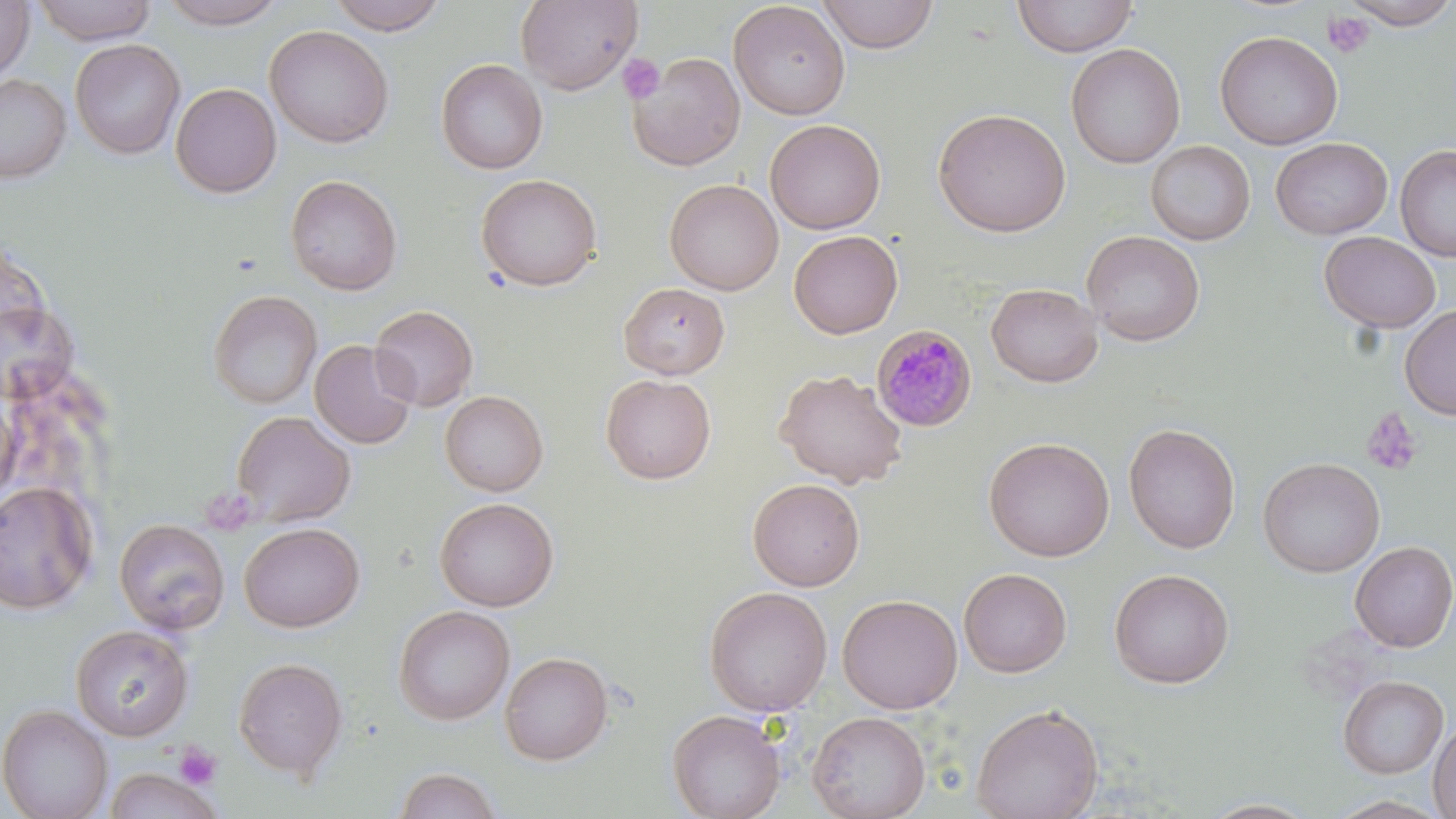
slide-level diagnosis = Plasmodium malariae
modality = optical microscopy
uninfected red blood cell locations = approximate bounding boxes as named x1/y1/x2/y2 corners in pixels: (x1=31, y1=0, x2=158, y2=45), (x1=155, y1=0, x2=288, y2=29), (x1=326, y1=0, x2=450, y2=35), (x1=515, y1=0, x2=641, y2=94), (x1=817, y1=0, x2=940, y2=53), (x1=1012, y1=0, x2=1138, y2=57), (x1=1342, y1=0, x2=1456, y2=29), (x1=0, y1=1, x2=34, y2=83), (x1=728, y1=1, x2=850, y2=120), (x1=264, y1=24, x2=394, y2=149), (x1=1214, y1=30, x2=1343, y2=150), (x1=70, y1=39, x2=185, y2=159), (x1=1066, y1=43, x2=1185, y2=168), (x1=628, y1=52, x2=746, y2=171), (x1=436, y1=59, x2=548, y2=174), (x1=0, y1=73, x2=71, y2=183), (x1=170, y1=82, x2=281, y2=198), (x1=932, y1=108, x2=1071, y2=237), (x1=765, y1=119, x2=885, y2=234), (x1=1270, y1=137, x2=1392, y2=239), (x1=1145, y1=140, x2=1255, y2=245), (x1=1395, y1=144, x2=1456, y2=263), (x1=476, y1=173, x2=603, y2=291), (x1=284, y1=174, x2=403, y2=295), (x1=665, y1=179, x2=783, y2=295), (x1=789, y1=230, x2=902, y2=339), (x1=1081, y1=230, x2=1205, y2=347), (x1=1319, y1=231, x2=1441, y2=333), (x1=618, y1=282, x2=730, y2=379), (x1=986, y1=283, x2=1103, y2=387), (x1=207, y1=289, x2=322, y2=409), (x1=0, y1=300, x2=79, y2=404), (x1=1399, y1=304, x2=1456, y2=420), (x1=370, y1=305, x2=478, y2=411), (x1=309, y1=339, x2=417, y2=449), (x1=774, y1=368, x2=908, y2=489), (x1=600, y1=373, x2=716, y2=484), (x1=440, y1=390, x2=548, y2=496), (x1=0, y1=394, x2=20, y2=509), (x1=231, y1=410, x2=355, y2=526), (x1=1123, y1=423, x2=1240, y2=554), (x1=984, y1=436, x2=1115, y2=562), (x1=1258, y1=457, x2=1385, y2=578), (x1=747, y1=478, x2=865, y2=591), (x1=0, y1=481, x2=99, y2=615), (x1=434, y1=497, x2=559, y2=611), (x1=114, y1=518, x2=230, y2=634), (x1=238, y1=522, x2=365, y2=633), (x1=1350, y1=541, x2=1456, y2=652), (x1=958, y1=567, x2=1072, y2=678), (x1=1109, y1=569, x2=1234, y2=688), (x1=703, y1=586, x2=832, y2=716), (x1=837, y1=594, x2=963, y2=714), (x1=393, y1=605, x2=515, y2=725), (x1=70, y1=624, x2=194, y2=741), (x1=499, y1=651, x2=613, y2=765), (x1=233, y1=657, x2=348, y2=780), (x1=1338, y1=675, x2=1449, y2=778), (x1=971, y1=703, x2=1103, y2=819), (x1=0, y1=704, x2=114, y2=819), (x1=667, y1=709, x2=785, y2=819), (x1=807, y1=711, x2=930, y2=819), (x1=1428, y1=718, x2=1456, y2=818), (x1=102, y1=766, x2=223, y2=819), (x1=392, y1=767, x2=503, y2=819), (x1=1200, y1=797, x2=1320, y2=818)
stain = May-Grünwald-Giemsa
image size = 1456×819 pixels
platelet locations = approximate bounding boxes as named x1/y1/x2/y2 corners in pixels: (x1=1321, y1=11, x2=1375, y2=58), (x1=618, y1=54, x2=664, y2=104), (x1=1360, y1=407, x2=1423, y2=476), (x1=174, y1=742, x2=222, y2=789)
preparation = thin blood film
field of view = single
magnification = 1000x
Plasmodium malariae-infected red blood cell locations = approximate bounding boxes as named x1/y1/x2/y2 corners in pixels: (x1=871, y1=325, x2=977, y2=432)